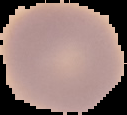
result = negative for malaria parasites
image type = cell region segmented out of the field of view; surrounding area masked to black
preparation = thin blood smear
image size = 127×115 pixels